Locate every blood parasite and identify its species.
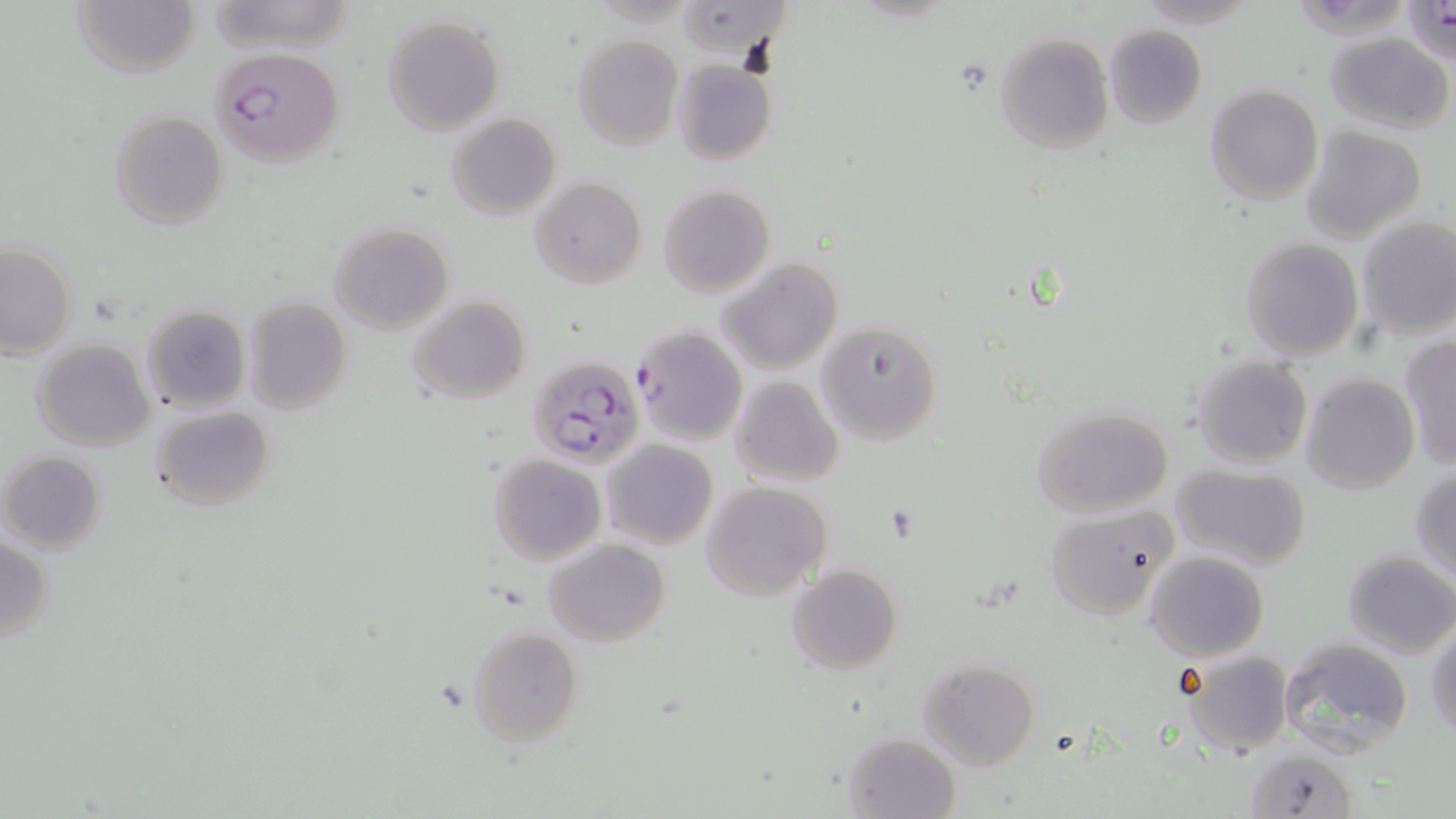

Approximate bounding boxes as (x1, y1, x2, y2) in pixels.
Plasmodium falciparum-infected red blood cells: (211, 47, 344, 166), (530, 355, 645, 467).
No Plasmodium ovale, Plasmodium malariae, Plasmodium vivax, Babesia divergens, or Trypanosoma brucei observed.

slide_level_diagnosis: Plasmodium falciparum
field_of_view: single
magnification: 1000x
image_size: 1456×819 pixels
stain: May-Grünwald-Giemsa
uninfected_red_blood_cell_locations: 'approximate bounding boxes as (x1, y1, x2, y2) in pixels: (71, 0, 202, 78), (678, 0, 794, 59), (1131, 0, 1263, 28), (204, 2, 356, 54), (1403, 2, 1454, 61), (382, 13, 506, 135), (1103, 25, 1207, 129), (995, 32, 1114, 155), (1324, 32, 1454, 133), (572, 35, 684, 148), (672, 60, 776, 166), (1203, 85, 1324, 206), (109, 109, 228, 228), (446, 113, 561, 219), (1300, 126, 1428, 244), (530, 176, 647, 288), (658, 184, 774, 297), (1356, 216, 1456, 339), (328, 222, 453, 333), (1240, 237, 1364, 361), (0, 244, 77, 359), (717, 257, 842, 375), (407, 295, 533, 404), (243, 297, 351, 416), (141, 304, 252, 414), (815, 320, 943, 446), (631, 326, 748, 445), (1398, 337, 1456, 471), (32, 338, 156, 451), (1192, 354, 1313, 469), (1300, 373, 1420, 494), (730, 375, 844, 486), (150, 405, 275, 511), (1031, 405, 1174, 517), (602, 439, 718, 549), (1, 451, 107, 552), (489, 455, 606, 565), (1171, 462, 1313, 570), (1409, 467, 1456, 583), (702, 481, 832, 600), (1044, 505, 1177, 621), (0, 537, 54, 640), (544, 539, 670, 645), (1144, 551, 1270, 660), (1341, 551, 1456, 658), (788, 564, 903, 674), (1427, 622, 1456, 741), (466, 627, 583, 746), (1279, 635, 1414, 759), (1179, 650, 1296, 756), (917, 658, 1039, 771), (844, 731, 961, 819), (1244, 746, 1359, 818)'
preparation: thin blood smear
modality: light microscopy